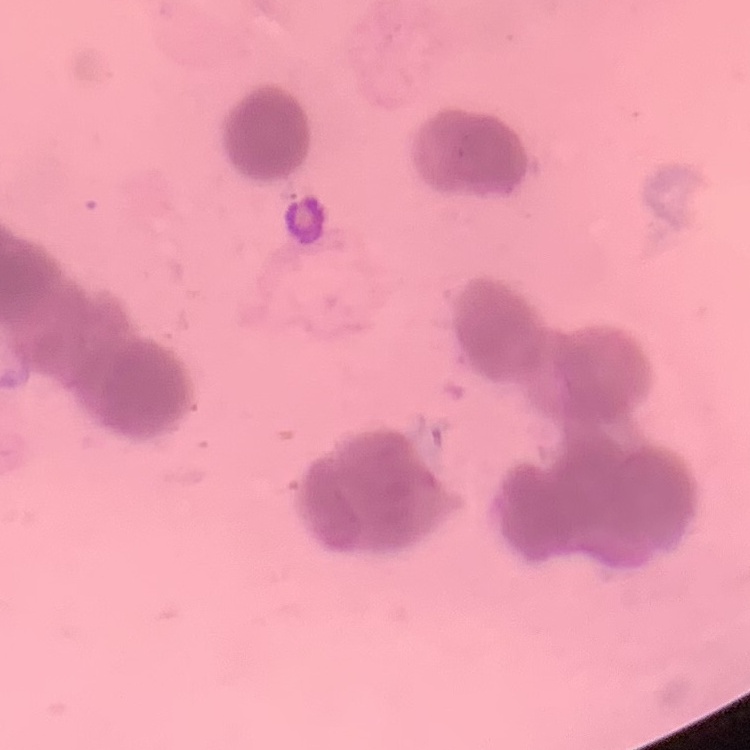

red blood cell morphology = rouleaux formation
preparation = thin peripheral smear
stain = Field's or Giemsa
image type = one tile cut from a larger photomicrograph